State which parasite is depicted.
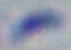
This is Toxoplasma gondii.

Summary:
  - Magnification: 1000x
  - Modality: micrograph